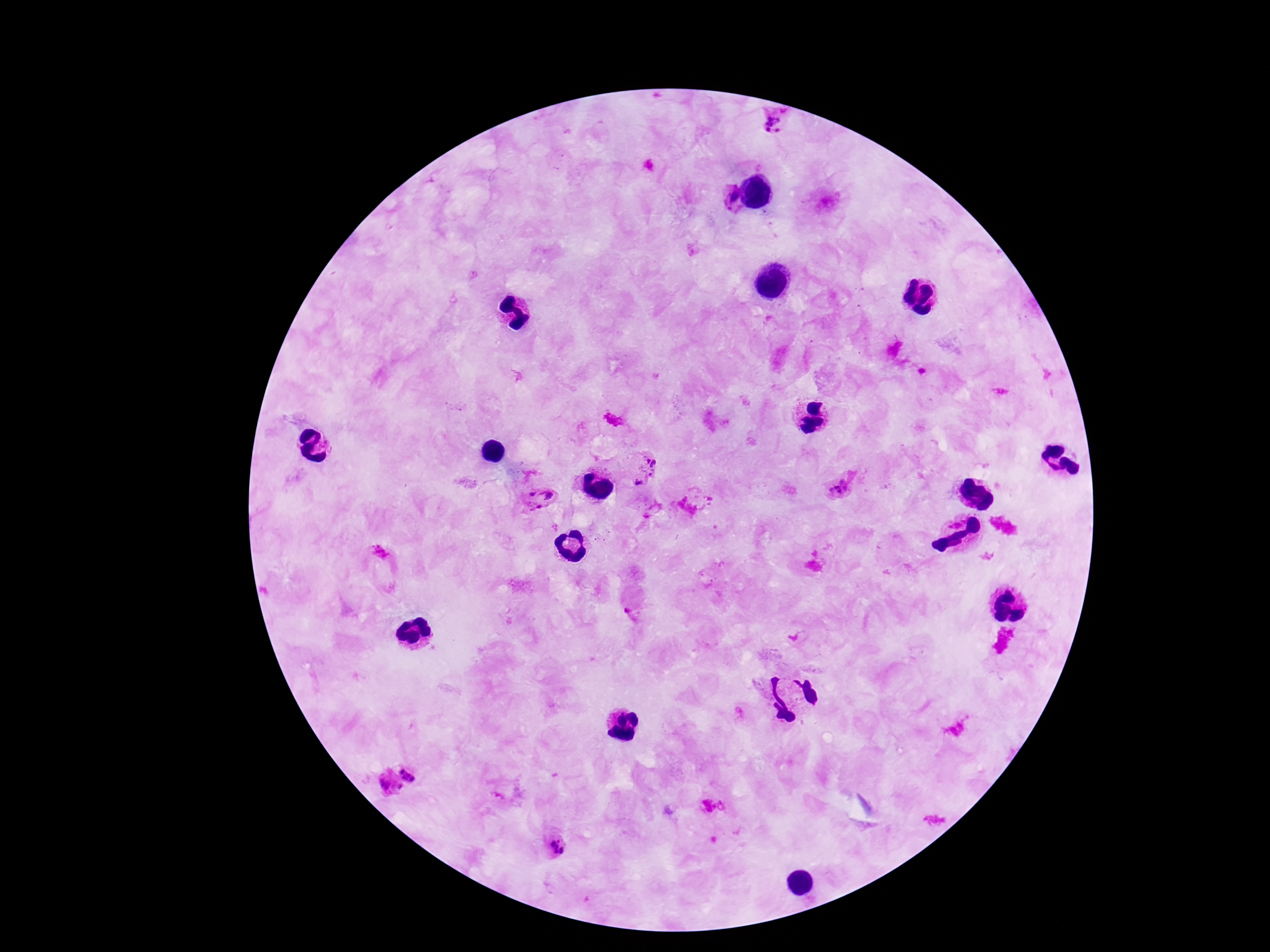

Approximate centers as [x, y] in pixels. Plasmodium parasite locations: [777, 119], [725, 198], [649, 465], [640, 482], [840, 488], [540, 497], [411, 772], [387, 786], [707, 806], [723, 806], [557, 846]. Single field of view. Image is 1270×952 pixels. Giemsa stain. Patient malaria status: infected. 100x magnification. Photographed through the microscope eyepiece with a smartphone camera. Thick peripheral-blood smear.